Point out each Plasmodium parasite.
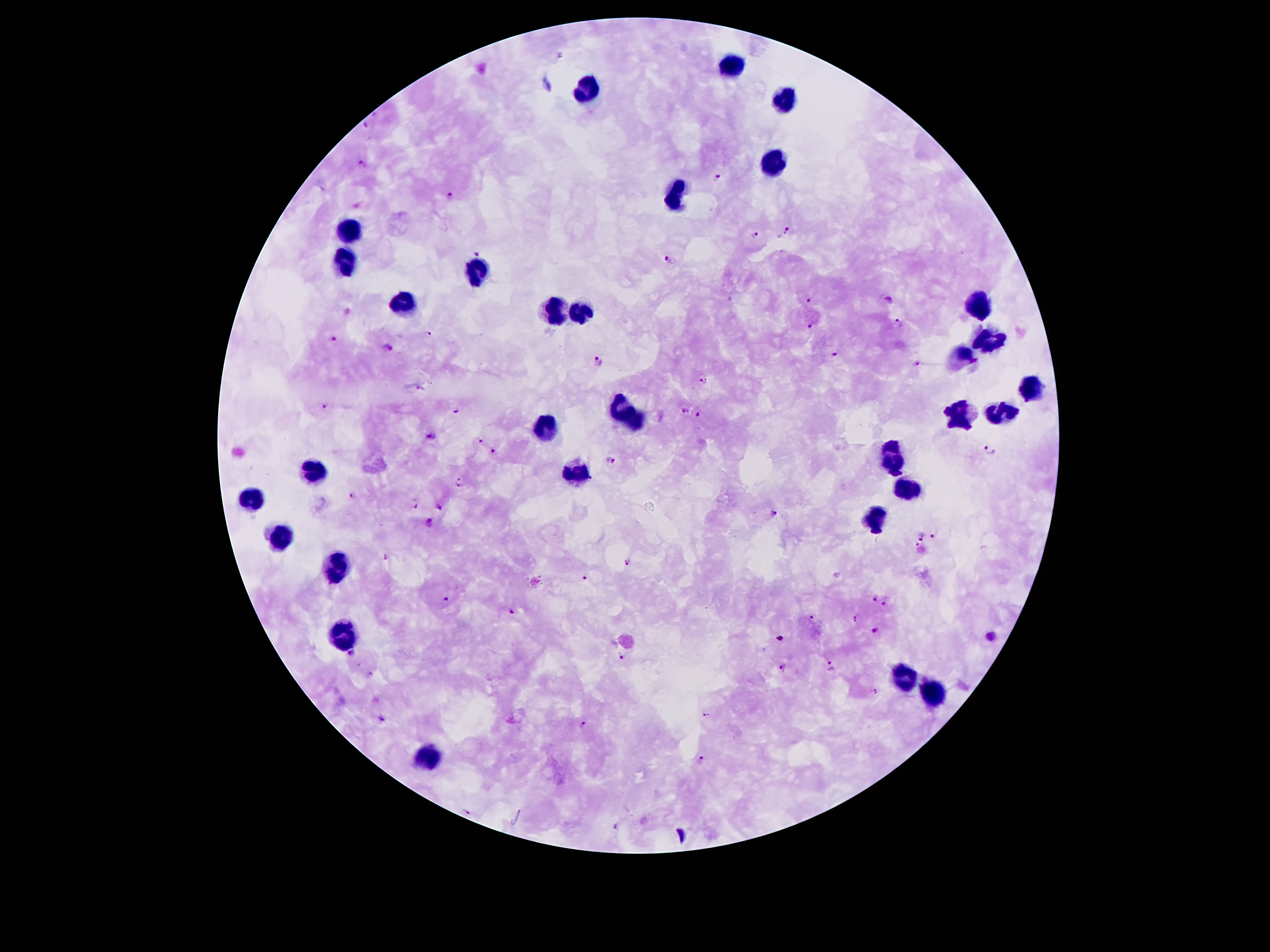

Approximate centers as {x, y} in pixels.
Plasmodium parasites: {362, 162}, {716, 179}, {448, 194}, {786, 230}, {755, 237}, {478, 251}, {668, 259}, {808, 299}, {899, 322}, {812, 324}, {430, 335}, {332, 339}, {388, 349}, {835, 353}, {597, 361}, {918, 365}, {704, 381}, {325, 406}, {456, 410}, {686, 412}, {698, 415}, {431, 436}, {481, 440}, {989, 451}, {494, 452}, {611, 459}, {459, 482}, {351, 495}, {416, 506}, {440, 507}, {774, 512}, {430, 524}, {935, 535}, {922, 536}, {386, 555}, {628, 565}, {586, 578}, {447, 597}, {876, 597}, {884, 604}, {512, 610}, {813, 616}, {857, 617}, {875, 629}, {989, 636}, {780, 639}, {351, 655}, {621, 657}, {831, 666}, {784, 667}, {372, 673}, {876, 691}, {707, 715}, {382, 718}, {584, 723}, {700, 759}, {468, 810}, {616, 827}.

leukocyte locations = {732, 63}, {585, 89}, {786, 95}, {771, 162}, {676, 196}, {351, 228}, {346, 261}, {477, 271}, {406, 302}, {979, 304}, {557, 311}, {585, 311}, {990, 343}, {962, 354}, {1028, 390}, {621, 405}, {961, 412}, {1000, 413}, {638, 421}, {544, 429}, {893, 447}, {886, 461}, {900, 462}, {314, 468}, {579, 469}, {896, 472}, {910, 489}, {255, 502}, {878, 511}, {878, 522}, {279, 534}, {339, 564}, {344, 638}, {904, 677}, {935, 692}, {428, 755}
field of view = single
magnification = 100x
image size = 1270×952 pixels
patient malaria status = infected with Plasmodium falciparum
stain = Giemsa
capture = smartphone through the microscope eyepiece
preparation = thick blood smear